State which cell type is depicted.
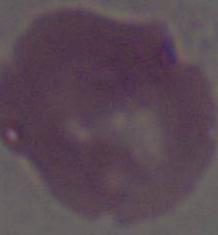
An erythrocyte.

Summary:
  - Magnification: 1000x
  - Modality: micrograph